Comment on the morphology of the red blood cells.
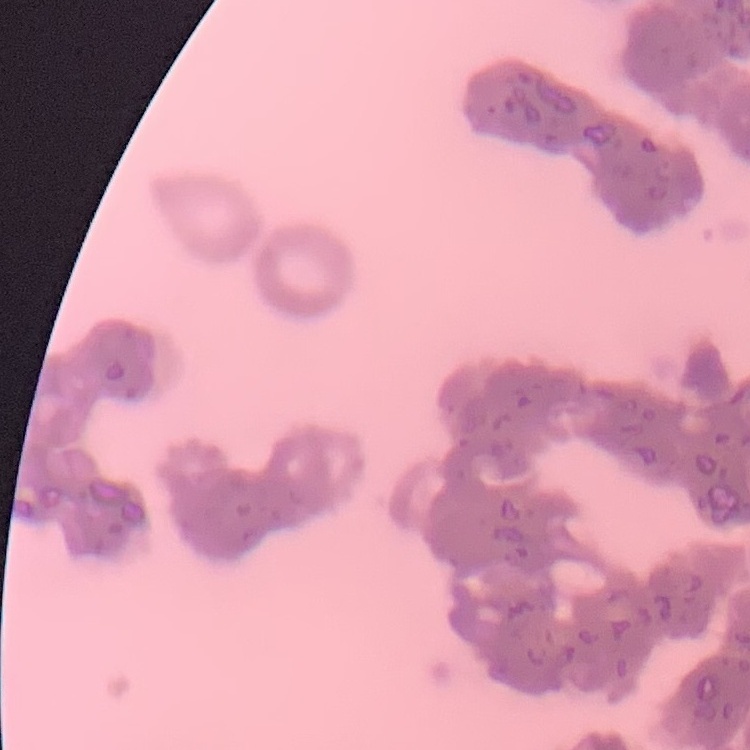

Rouleaux formation.

One tile cut from a larger photomicrograph. Stained with either Field's or Giemsa. Thin blood film.